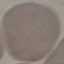 Result: negative for malaria parasites. Thin blood smear. Cell patch, automatically extracted from a larger field of view and resized to 64 × 64 pixels. Acquired by smartphone through the microscope eyepiece. Giemsa-stained preparation.